Assess this cell for malaria.
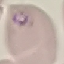

It is parasitized.

capture = smartphone camera at the microscope eyepiece
preparation = thin smear
stain = Giemsa
image type = cell patch, automatically extracted from a larger field of view and resized to 64 × 64 pixels